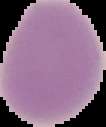

Summary:
  - Preparation: thin blood smear
  - Image size: 106×127 pixels
  - Image type: cell region segmented out of the field of view; surrounding area masked to black
  - Result: negative for Plasmodium parasites